State the preparation type.
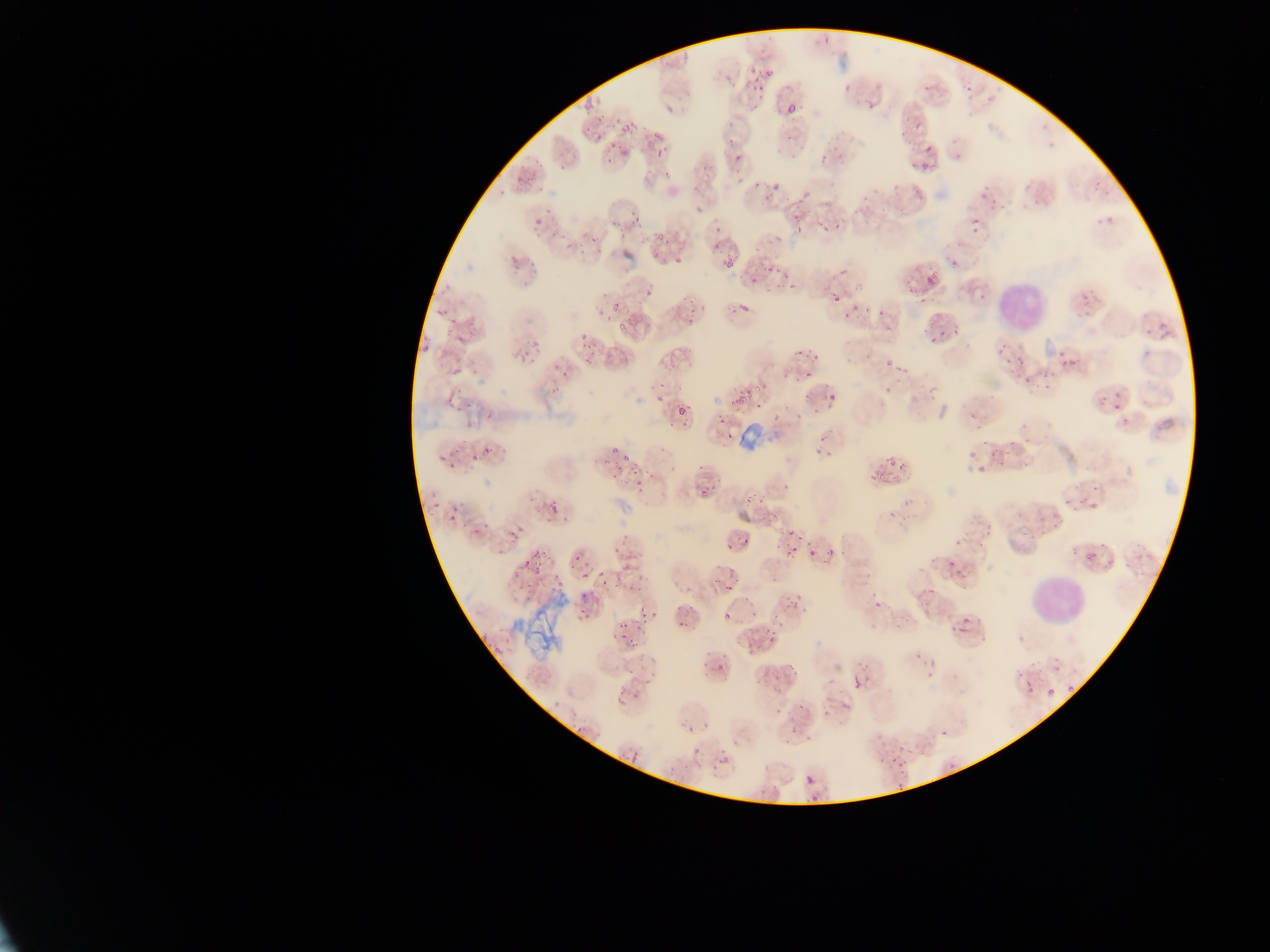
Thin blood smear.

Approximate bounding boxes as {left, top, right, bottom} in pixels. Leukocyte locations: {989, 270, 1043, 322}, {1034, 578, 1082, 635}. Plasmodium parasite locations: {750, 69, 763, 85}, {753, 85, 764, 93}, {787, 103, 798, 113}, {622, 124, 634, 131}, {912, 124, 922, 134}, {653, 129, 662, 140}, {607, 141, 616, 151}, {923, 145, 934, 152}, {655, 148, 666, 156}, {734, 156, 745, 160}, {920, 164, 938, 172}, {535, 216, 544, 226}, {836, 222, 841, 230}, {795, 224, 803, 232}, {821, 225, 829, 233}, {714, 226, 723, 235}, {655, 232, 665, 242}, {713, 244, 721, 252}, {510, 257, 520, 270}, {673, 257, 685, 268}, {726, 258, 736, 270}, {766, 267, 774, 275}, {928, 270, 937, 280}, {752, 275, 759, 285}, {924, 277, 935, 288}, {646, 286, 655, 298}, {610, 299, 623, 309}, {739, 303, 750, 317}, {436, 307, 449, 315}, {643, 314, 650, 323}, {688, 317, 694, 327}, {448, 320, 460, 327}, {618, 323, 629, 335}, {952, 330, 961, 336}, {580, 333, 590, 341}, {928, 334, 937, 345}, {421, 345, 429, 355}, {895, 365, 908, 373}, {450, 368, 460, 379}, {752, 384, 762, 392}, {739, 394, 747, 406}, {447, 397, 455, 410}, {728, 398, 738, 405}, {676, 407, 688, 416}, {486, 411, 494, 419}, {483, 448, 490, 456}, {610, 448, 619, 454}, {438, 452, 450, 462}, {623, 453, 630, 462}, {471, 455, 479, 464}, {447, 462, 455, 469}, {898, 462, 909, 473}, {631, 466, 640, 479}, {878, 472, 887, 480}, {893, 476, 903, 485}, {636, 479, 646, 488}, {700, 490, 708, 497}, {430, 500, 441, 510}, {450, 501, 458, 511}, {547, 501, 559, 513}, {470, 526, 483, 536}, {786, 530, 797, 538}, {508, 531, 518, 540}, {741, 538, 749, 544}, {725, 543, 734, 550}, {788, 544, 799, 556}, {824, 546, 837, 557}, {534, 549, 547, 560}, {1083, 553, 1093, 561}, {524, 557, 532, 566}, {530, 566, 543, 575}, {596, 572, 605, 579}, {580, 573, 588, 583}, {626, 582, 635, 589}, {724, 584, 734, 591}, {580, 596, 588, 603}, {639, 605, 657, 621}, {578, 610, 588, 619}, {723, 612, 731, 618}, {960, 616, 970, 625}, {679, 621, 689, 625}, {618, 625, 628, 630}, {960, 626, 970, 634}, {765, 630, 778, 639}, {628, 640, 641, 647}, {492, 646, 501, 655}, {747, 648, 755, 655}, {787, 661, 795, 667}, {852, 677, 859, 692}, {1024, 680, 1037, 694}, {1065, 686, 1076, 696}, {1045, 689, 1057, 696}, {632, 691, 644, 700}, {693, 746, 702, 757}, {630, 751, 643, 764}, {720, 757, 732, 765}, {895, 762, 904, 769}, {806, 775, 814, 787}, {811, 795, 820, 805} | approximate {x, y} pixel centers of objects too small to bound: {691, 310}, {660, 400}, {891, 462}, {451, 519}, {810, 553}, {576, 559}, {602, 584}, {638, 629}, {622, 636}, {720, 666}, {801, 706}. Artifact (stain precipitate or debris) locations: {735, 424, 763, 449}, {512, 597, 566, 653}. Photographed through a microscope with a mobile-phone camera. Image is 1270×952 pixels. Sample from Ghana. One field of view.